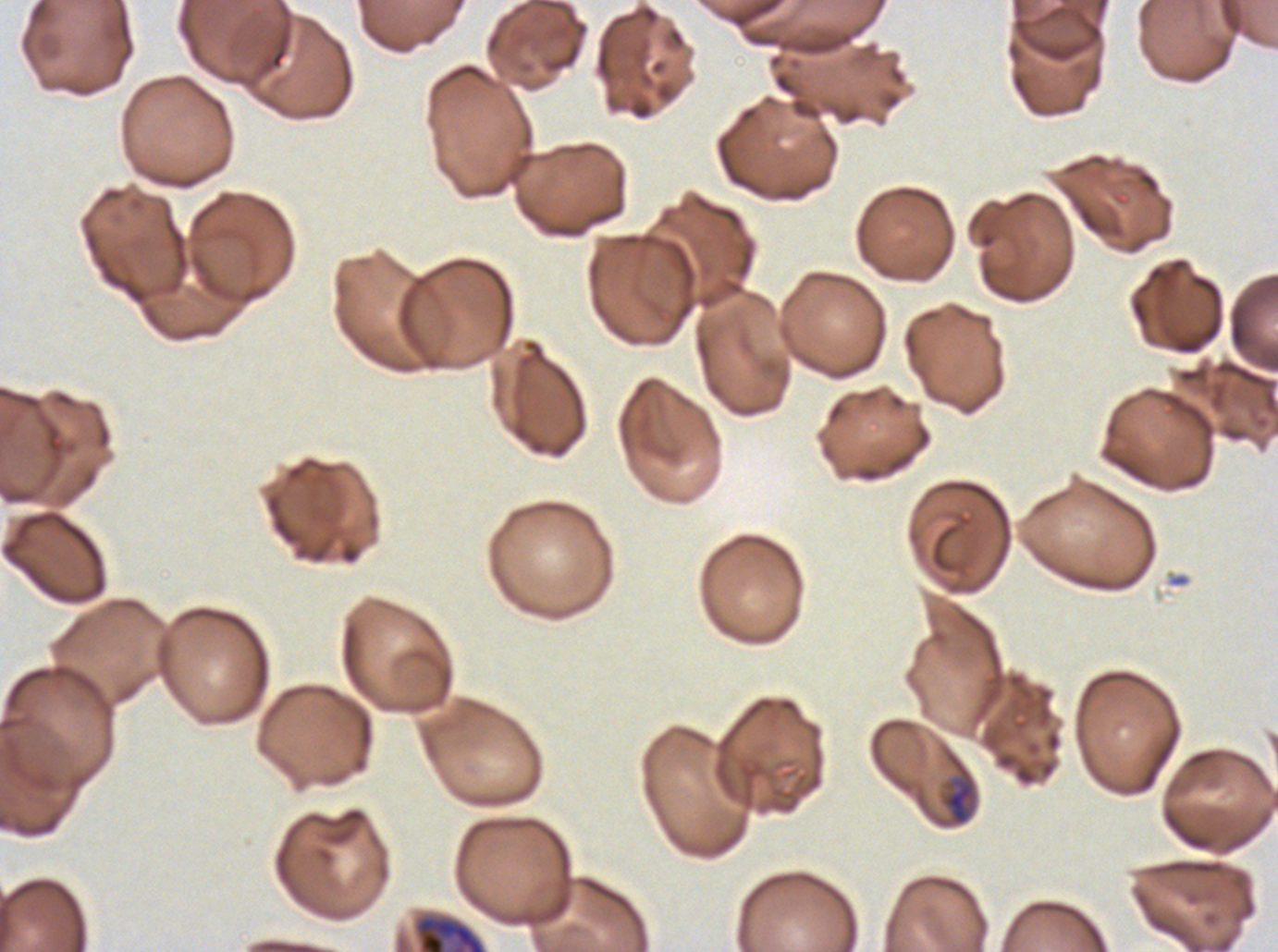 Approximate bounding rectangles given as corner coordinates in pixels from the top-left. Early schizont locations: (x1=412, y1=912, x2=487, y2=951). Mid trophozoite locations: (x1=942, y1=776, x2=976, y2=825). Image is 1278×952 pixels. Life-cycle stages observed: mid trophozoite, early schizont. One sub-image of a larger composite. Thin blood smear. Ex-vivo Plasmodium falciparum culture from a patient in The Gambia, grown for 24 to 48 hours. Giemsa stain.